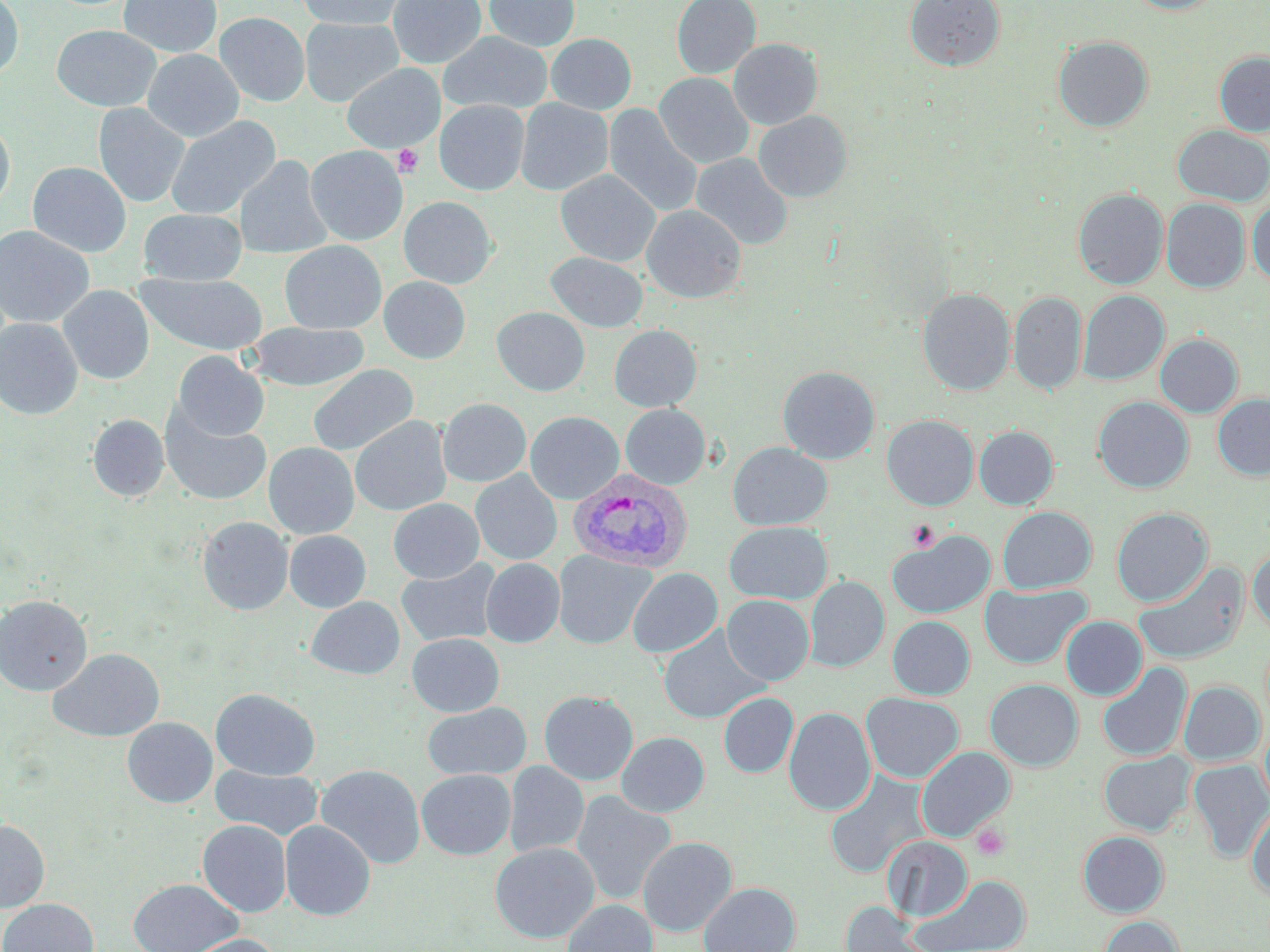

Summary:
  - Coordinate format: approximate bounding boxes as named x1/y1/x2/y2 corners in pixels
  - Uninfected red blood cell locations: (x1=0, y1=0, x2=24, y2=80), (x1=119, y1=0, x2=222, y2=58), (x1=387, y1=0, x2=487, y2=68), (x1=484, y1=0, x2=579, y2=51), (x1=671, y1=0, x2=761, y2=79), (x1=904, y1=0, x2=1006, y2=71), (x1=1123, y1=0, x2=1226, y2=14), (x1=296, y1=1, x2=409, y2=30), (x1=214, y1=12, x2=310, y2=106), (x1=300, y1=17, x2=404, y2=107), (x1=51, y1=25, x2=161, y2=111), (x1=438, y1=31, x2=553, y2=115), (x1=546, y1=33, x2=636, y2=114), (x1=1053, y1=35, x2=1153, y2=132), (x1=728, y1=38, x2=823, y2=130), (x1=143, y1=49, x2=244, y2=142), (x1=1214, y1=51, x2=1270, y2=136), (x1=342, y1=63, x2=445, y2=152), (x1=654, y1=72, x2=754, y2=168), (x1=515, y1=98, x2=613, y2=195), (x1=434, y1=100, x2=530, y2=195), (x1=93, y1=102, x2=190, y2=207), (x1=603, y1=104, x2=703, y2=217), (x1=754, y1=110, x2=852, y2=202), (x1=165, y1=116, x2=281, y2=220), (x1=0, y1=119, x2=15, y2=212), (x1=1172, y1=125, x2=1270, y2=206), (x1=305, y1=145, x2=408, y2=245), (x1=691, y1=152, x2=793, y2=250), (x1=235, y1=155, x2=333, y2=259), (x1=27, y1=162, x2=131, y2=257), (x1=555, y1=169, x2=660, y2=266), (x1=1073, y1=188, x2=1169, y2=289), (x1=399, y1=196, x2=498, y2=289), (x1=1161, y1=199, x2=1250, y2=293), (x1=1248, y1=201, x2=1270, y2=285), (x1=641, y1=204, x2=746, y2=303), (x1=139, y1=208, x2=247, y2=286), (x1=0, y1=225, x2=95, y2=329), (x1=279, y1=240, x2=386, y2=334), (x1=546, y1=252, x2=648, y2=332), (x1=135, y1=273, x2=268, y2=355), (x1=378, y1=276, x2=471, y2=363), (x1=58, y1=285, x2=155, y2=385), (x1=917, y1=288, x2=1016, y2=395), (x1=1078, y1=290, x2=1169, y2=384), (x1=1009, y1=291, x2=1086, y2=395), (x1=492, y1=306, x2=590, y2=396), (x1=0, y1=318, x2=83, y2=419), (x1=245, y1=322, x2=369, y2=391), (x1=609, y1=324, x2=702, y2=411), (x1=1155, y1=333, x2=1243, y2=417), (x1=172, y1=350, x2=269, y2=441), (x1=307, y1=364, x2=418, y2=456), (x1=777, y1=366, x2=880, y2=464), (x1=1212, y1=393, x2=1270, y2=480), (x1=1093, y1=396, x2=1194, y2=493), (x1=437, y1=398, x2=531, y2=487), (x1=620, y1=404, x2=710, y2=489), (x1=160, y1=406, x2=272, y2=506), (x1=525, y1=410, x2=624, y2=503), (x1=88, y1=414, x2=169, y2=501), (x1=350, y1=415, x2=452, y2=516), (x1=882, y1=415, x2=978, y2=510), (x1=974, y1=425, x2=1058, y2=509), (x1=263, y1=442, x2=359, y2=539), (x1=727, y1=442, x2=832, y2=530), (x1=471, y1=470, x2=562, y2=565), (x1=388, y1=498, x2=484, y2=583), (x1=997, y1=506, x2=1097, y2=594), (x1=1111, y1=507, x2=1213, y2=607), (x1=197, y1=516, x2=294, y2=615), (x1=724, y1=521, x2=832, y2=604), (x1=284, y1=530, x2=371, y2=612), (x1=887, y1=530, x2=996, y2=619), (x1=1248, y1=547, x2=1270, y2=635), (x1=553, y1=550, x2=655, y2=649), (x1=481, y1=558, x2=565, y2=647), (x1=396, y1=559, x2=503, y2=647), (x1=1133, y1=561, x2=1249, y2=664), (x1=628, y1=567, x2=723, y2=657), (x1=805, y1=576, x2=889, y2=671), (x1=979, y1=582, x2=1091, y2=669), (x1=0, y1=594, x2=92, y2=695), (x1=722, y1=594, x2=814, y2=685), (x1=306, y1=597, x2=405, y2=679), (x1=887, y1=616, x2=975, y2=699), (x1=1061, y1=616, x2=1147, y2=700), (x1=658, y1=628, x2=769, y2=724), (x1=407, y1=633, x2=504, y2=717), (x1=49, y1=648, x2=164, y2=741), (x1=1097, y1=662, x2=1191, y2=761), (x1=985, y1=678, x2=1083, y2=771), (x1=1179, y1=681, x2=1264, y2=765), (x1=211, y1=688, x2=320, y2=780), (x1=539, y1=690, x2=638, y2=785), (x1=718, y1=692, x2=798, y2=778), (x1=860, y1=692, x2=964, y2=782), (x1=422, y1=702, x2=532, y2=781), (x1=783, y1=706, x2=875, y2=815), (x1=122, y1=717, x2=217, y2=807), (x1=1260, y1=723, x2=1270, y2=810), (x1=616, y1=731, x2=709, y2=817), (x1=916, y1=745, x2=1015, y2=841), (x1=1099, y1=750, x2=1194, y2=835), (x1=1189, y1=759, x2=1270, y2=862), (x1=505, y1=761, x2=589, y2=858), (x1=210, y1=764, x2=324, y2=841), (x1=315, y1=764, x2=426, y2=868), (x1=416, y1=769, x2=516, y2=859), (x1=824, y1=770, x2=930, y2=878), (x1=571, y1=790, x2=676, y2=906), (x1=1246, y1=802, x2=1270, y2=899), (x1=0, y1=819, x2=50, y2=913), (x1=197, y1=820, x2=291, y2=917), (x1=280, y1=820, x2=375, y2=920), (x1=1078, y1=830, x2=1169, y2=917), (x1=882, y1=835, x2=973, y2=922), (x1=637, y1=836, x2=737, y2=936), (x1=490, y1=841, x2=599, y2=942), (x1=909, y1=874, x2=1032, y2=952), (x1=129, y1=878, x2=242, y2=952), (x1=699, y1=881, x2=800, y2=952), (x1=0, y1=898, x2=99, y2=952), (x1=562, y1=899, x2=658, y2=952), (x1=841, y1=902, x2=931, y2=952), (x1=1096, y1=915, x2=1184, y2=952), (x1=183, y1=934, x2=280, y2=952)
  - Plasmodium vivax-infected red blood cell locations: (x1=568, y1=470, x2=693, y2=573)
  - Platelet locations: (x1=393, y1=144, x2=425, y2=177), (x1=906, y1=520, x2=939, y2=551), (x1=971, y1=823, x2=1011, y2=861)
  - Slide-level diagnosis: Plasmodium vivax
  - Magnification: 1000x
  - Stain: May-Grünwald-Giemsa
  - Preparation: thin blood film
  - Field of view: one of a larger specimen
  - Modality: optical microscopy
  - Image size: 1270×952 pixels